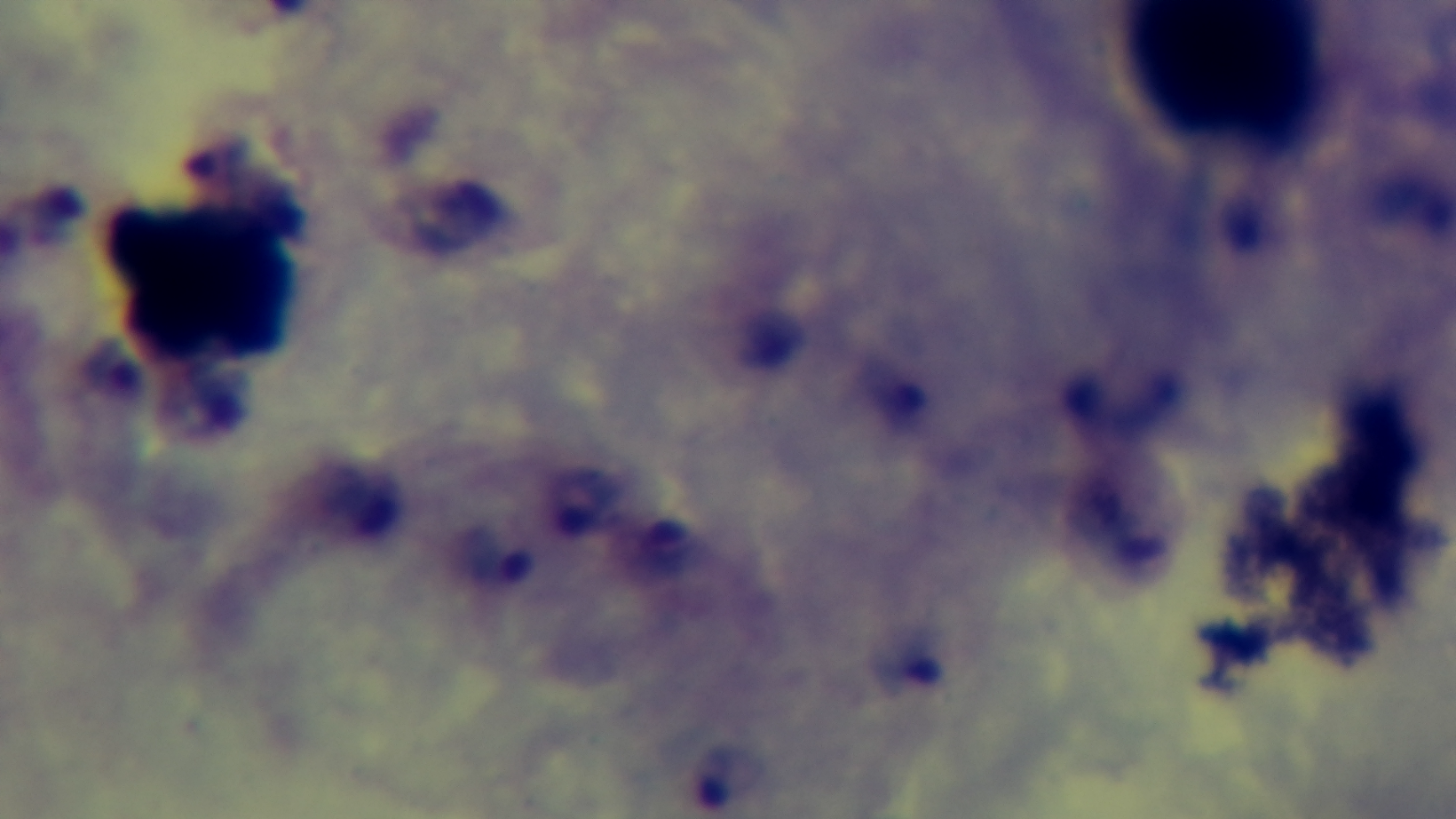

malaria status = positive
modality = light microscopy
capture = mounted 4K digital camera
stain = Giemsa
field of view = one from the slide
preparation = thick smear
objective = 100x oil immersion